Assess this cell for malaria.
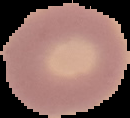

It is uninfected.

image_type: cell region segmented out of the field of view; surrounding area masked to black
image_size: 130×118 pixels
preparation: thin blood smear